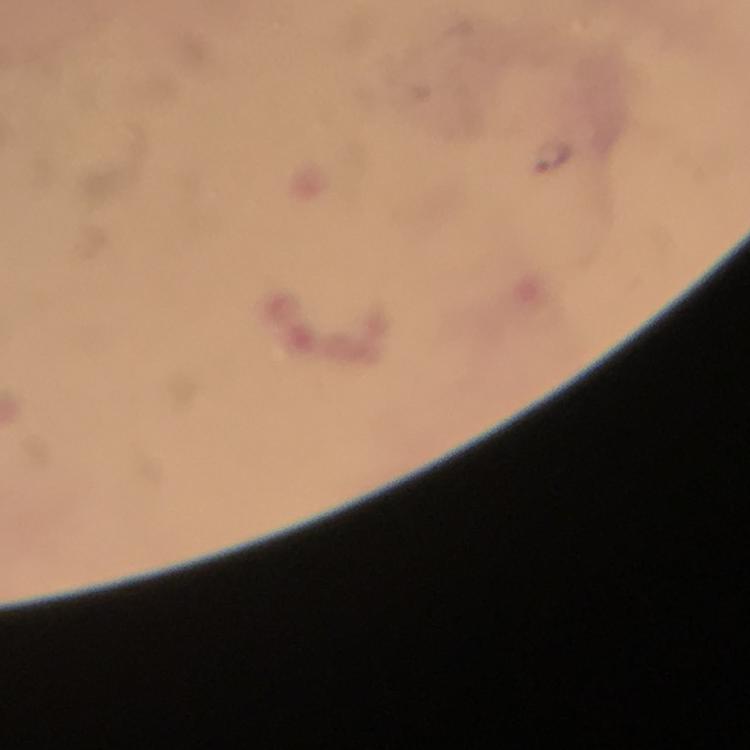

Approximate centers as (x, y) in pixels.
Summary:
  - Plasmodium parasite locations: (553, 154)
  - Magnification: 100x
  - Capture: smartphone photograph through a microscope
  - Context: from a diagnostic examination for malaria
  - Stain: Giemsa
  - Cropped from: a single field of view
  - Immersion oil: used
  - Preparation: thick smear
  - Image size: 750×750 pixels